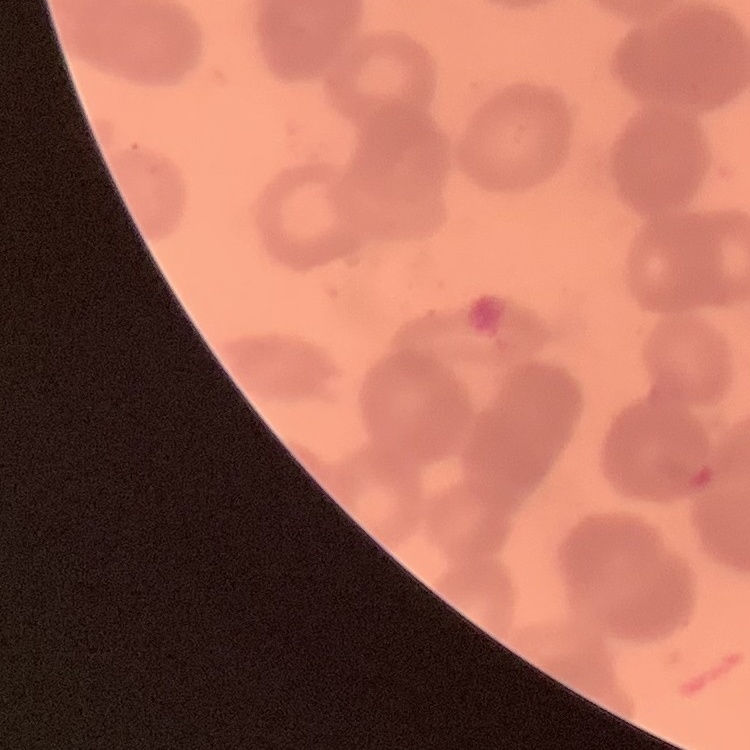

red_blood_cell_morphology: rouleaux formation
stain: Field's or Giemsa
preparation: thin blood smear
image_type: square crop of a larger photomicrograph